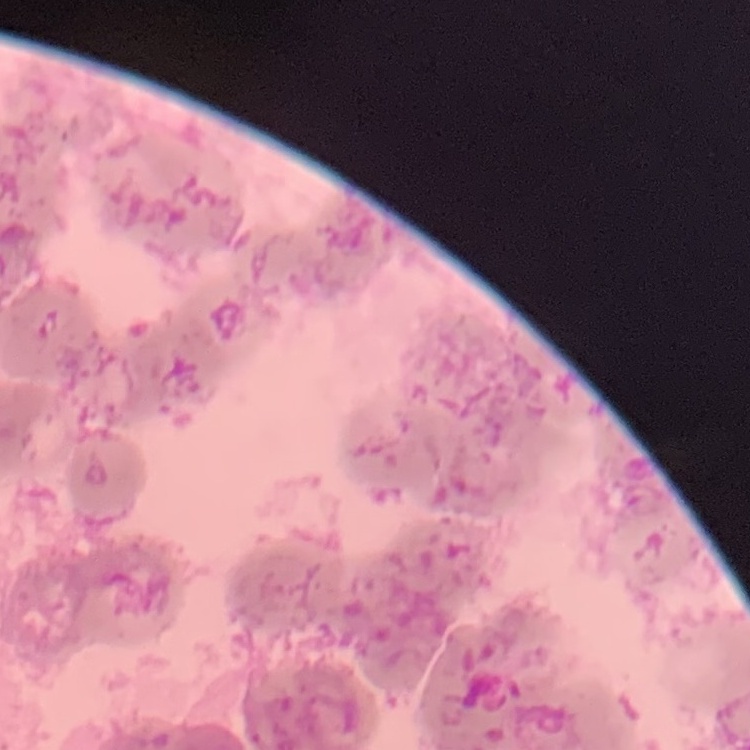 The red blood cells exhibit rouleaux formation. Square crop of a larger photomicrograph. Field's or Giemsa stain. Thin blood film.